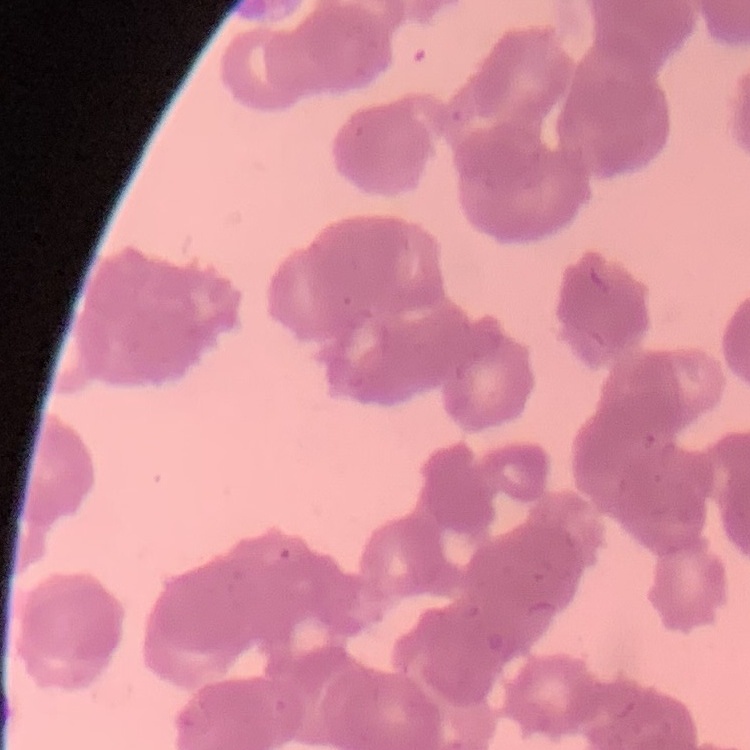
red blood cell morphology = rouleaux formation
preparation = thin blood film
image type = one tile cut from a larger photomicrograph
stain = Field's or Giemsa